Identify the blood parasite species.
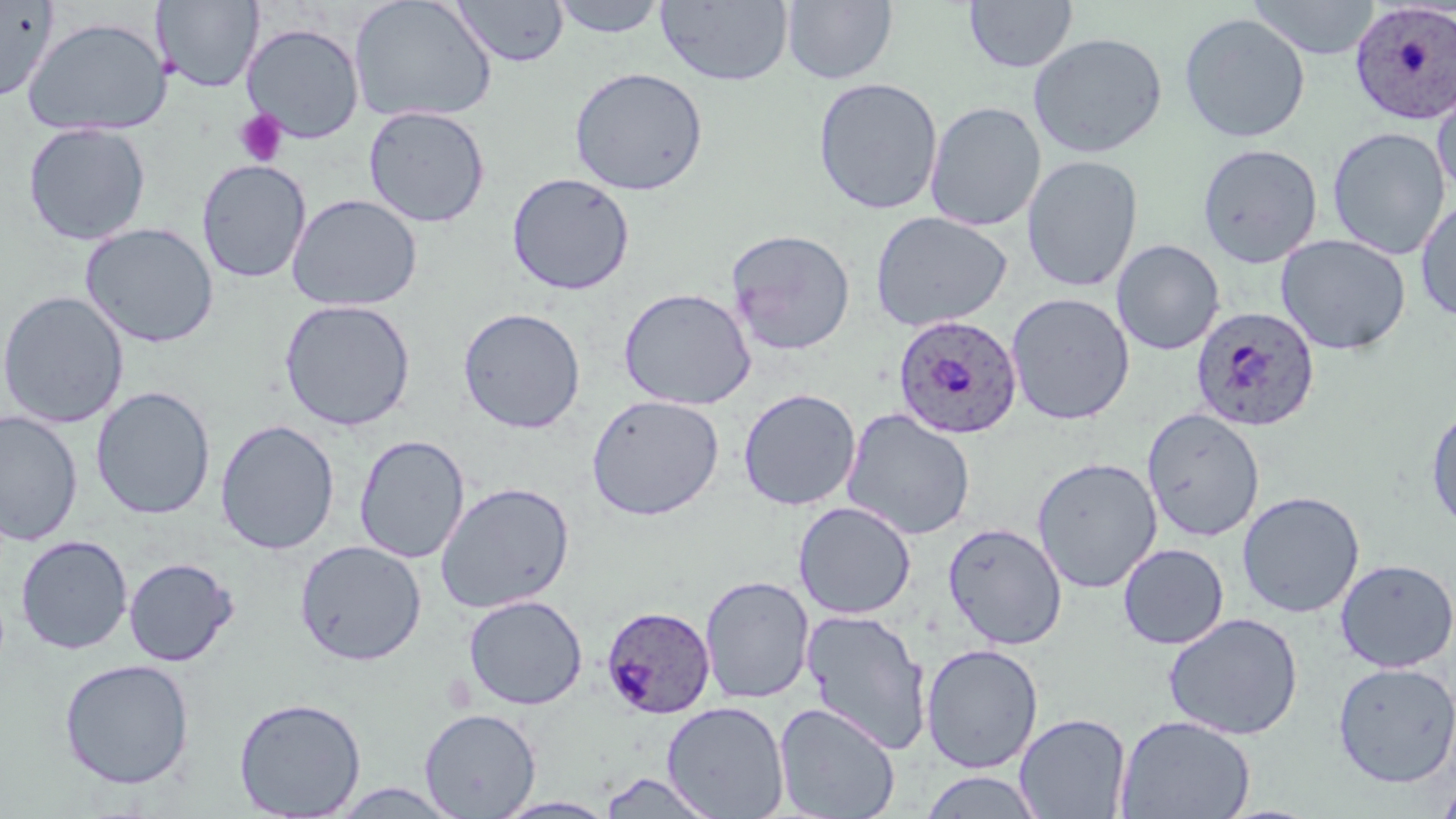

Plasmodium ovale.

stain = May-Grünwald-Giemsa
preparation = thin blood smear
image size = 1456×819 pixels
field of view = one of a larger specimen
uninfected red blood cell locations = approximate bounding boxes as (x1,y1)-(x2,y2) corner pairs in pixels: (152,0)-(264,93), (451,0)-(569,68), (548,0)-(670,38), (656,0)-(794,86), (781,0)-(898,85), (1248,0)-(1381,60), (0,1)-(58,103), (348,1)-(497,123), (964,1)-(1078,74), (1179,12)-(1311,144), (20,15)-(172,137), (242,23)-(365,143), (1028,32)-(1168,158), (569,66)-(709,196), (1431,72)-(1456,204), (812,77)-(944,215), (925,101)-(1047,232), (362,104)-(491,228), (22,123)-(151,245), (1327,126)-(1451,260), (1198,143)-(1323,268), (1022,154)-(1144,292), (196,159)-(312,283), (506,172)-(635,295), (286,194)-(423,312), (1415,197)-(1456,323), (870,210)-(1012,332), (79,222)-(220,348), (725,228)-(856,356), (1276,234)-(1412,355), (1111,239)-(1225,355), (618,287)-(756,410), (0,290)-(129,429), (1006,293)-(1135,425), (278,298)-(417,432), (458,307)-(586,433), (90,385)-(216,520), (738,388)-(861,511), (586,394)-(725,521), (1425,402)-(1456,536), (841,407)-(976,540), (1142,408)-(1265,542), (0,410)-(83,546), (214,419)-(340,555), (354,434)-(470,564), (1031,456)-(1163,593), (435,481)-(575,614), (1237,490)-(1365,618), (793,501)-(917,619), (943,521)-(1068,650), (15,534)-(133,654), (294,540)-(427,665), (1117,542)-(1229,650), (123,556)-(239,667), (1334,558)-(1456,672), (700,575)-(815,704), (463,594)-(588,710), (802,608)-(931,756), (1164,612)-(1303,740), (921,643)-(1043,774), (58,658)-(195,790), (1332,661)-(1456,788), (233,696)-(366,818), (661,701)-(790,818), (773,702)-(901,818), (419,708)-(541,818), (1014,712)-(1132,819), (1115,714)-(1255,819), (918,770)-(1047,818), (597,772)-(722,818), (1435,779)-(1456,819), (492,796)-(621,818)
magnification = 1000x
Plasmodium ovale-infected red blood cell locations = approximate bounding boxes as (x1,y1)-(x2,y2) corner pairs in pixels: (1349,2)-(1455,125), (1190,305)-(1321,432), (892,315)-(1023,439), (601,606)-(716,718)
platelet locations = approximate bounding boxes as (x1,y1)-(x2,y2) corner pairs in pixels: (234,109)-(288,167)
modality = optical microscopy